Comment on the morphology of the red blood cells.
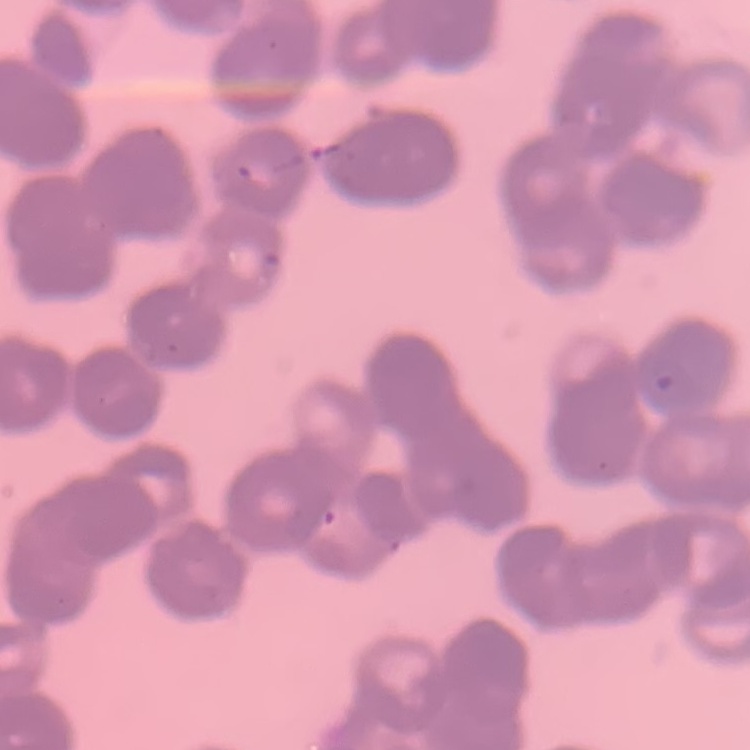

Rouleaux formation.

One tile cut from a larger photomicrograph. Stained with either Field's or Giemsa. Thin blood smear.